Assess the morphology of the red blood cells.
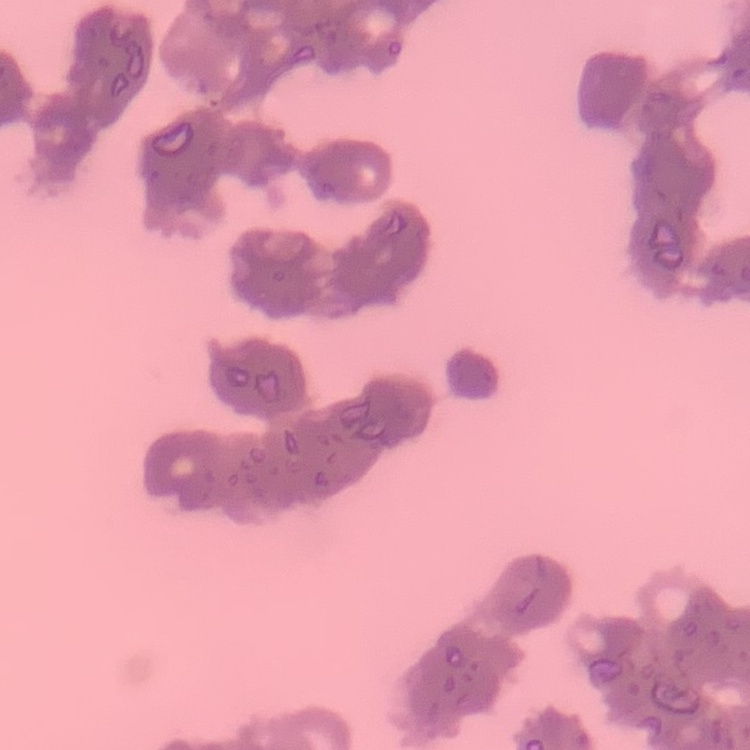
Rouleaux formation.

Thin peripheral smear. Stained with either Field's or Giemsa. Square crop of a larger photomicrograph.